State which parasite is depicted.
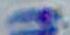
This is Toxoplasma gondii.

{
  "modality": "micrograph",
  "magnification": "1000x"
}